Identify the cell.
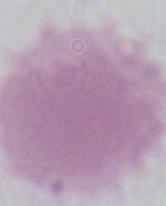

This is an erythrocyte.

modality = micrograph
magnification = 1000x